Classify this cell by malaria status.
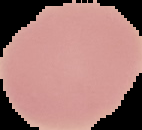
It is uninfected.

Segmented cell region on a black background. From a thin blood smear. Image is 142×130 pixels.